State which parasite is depicted.
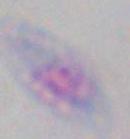

Toxoplasma gondii.

Captured at 1000x magnification. Photomicrograph.